Point out each leukocyte.
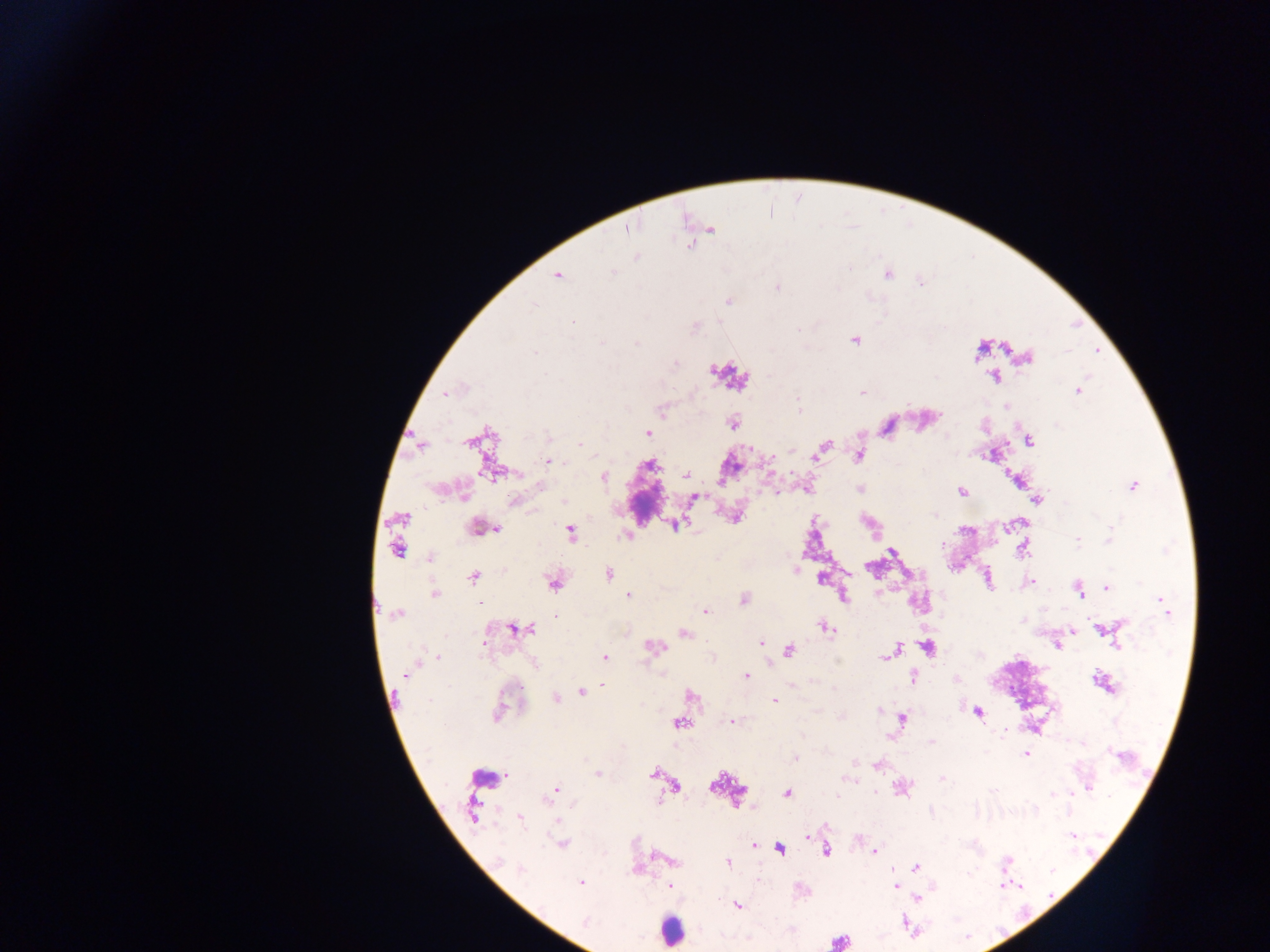

Approximate centers as x y in pixels.
Leukocytes: 671 930.
One object is labeled both malaria parasite and leukocyte by the source: 839 941.

Summary:
  - Malaria parasite locations: 710 229; 636 257; 886 273; 557 275; 919 282; 573 321; 854 339; 979 350; 1026 356; 995 376; 1077 390; 860 391; 445 393; 662 410; 732 422; 647 433; 1028 441; 822 446; 993 453; 858 455; 815 457; 548 461; 493 473; 685 475; 602 476; 1017 478; 1133 486; 860 489; 961 491; 693 497; 1036 499; 515 500; 734 517; 676 524; 481 528; 496 528; 569 532; 627 536; 1077 540; 397 547; 1023 547; 892 552; 430 557; 870 567; 608 573; 846 573; 473 577; 821 578; 987 579; 552 581; 1029 582; 1107 587; 1078 590; 433 594; 842 594; 628 595; 743 599; 1164 604; 705 612; 396 613; 824 627; 515 628; 1102 629; 1073 631; 683 633; 761 643; 1057 645; 652 647; 926 647; 894 649; 789 650; 439 655; 887 655; 604 657; 746 676; 912 677; 956 678; 1103 682; 600 686; 581 692; 690 694; 555 699; 774 701; 500 709; 497 712; 977 712; 902 719; 732 721; 679 723; 931 742; 1027 753; 795 758; 877 765; 597 773; 653 774; 674 786; 901 787; 1086 787; 556 790; 786 793; 473 809; 520 819; 557 821; 807 835; 562 844; 754 845; 779 848; 825 850; 874 851; 727 862; 915 867; 580 883; 669 885; 894 885; 917 898; 737 904
  - Image size: 1270×952 pixels
  - Field of view: single
  - Country: Ghana
  - Preparation: thick blood smear
  - Capture: mobile-phone photograph through a microscope